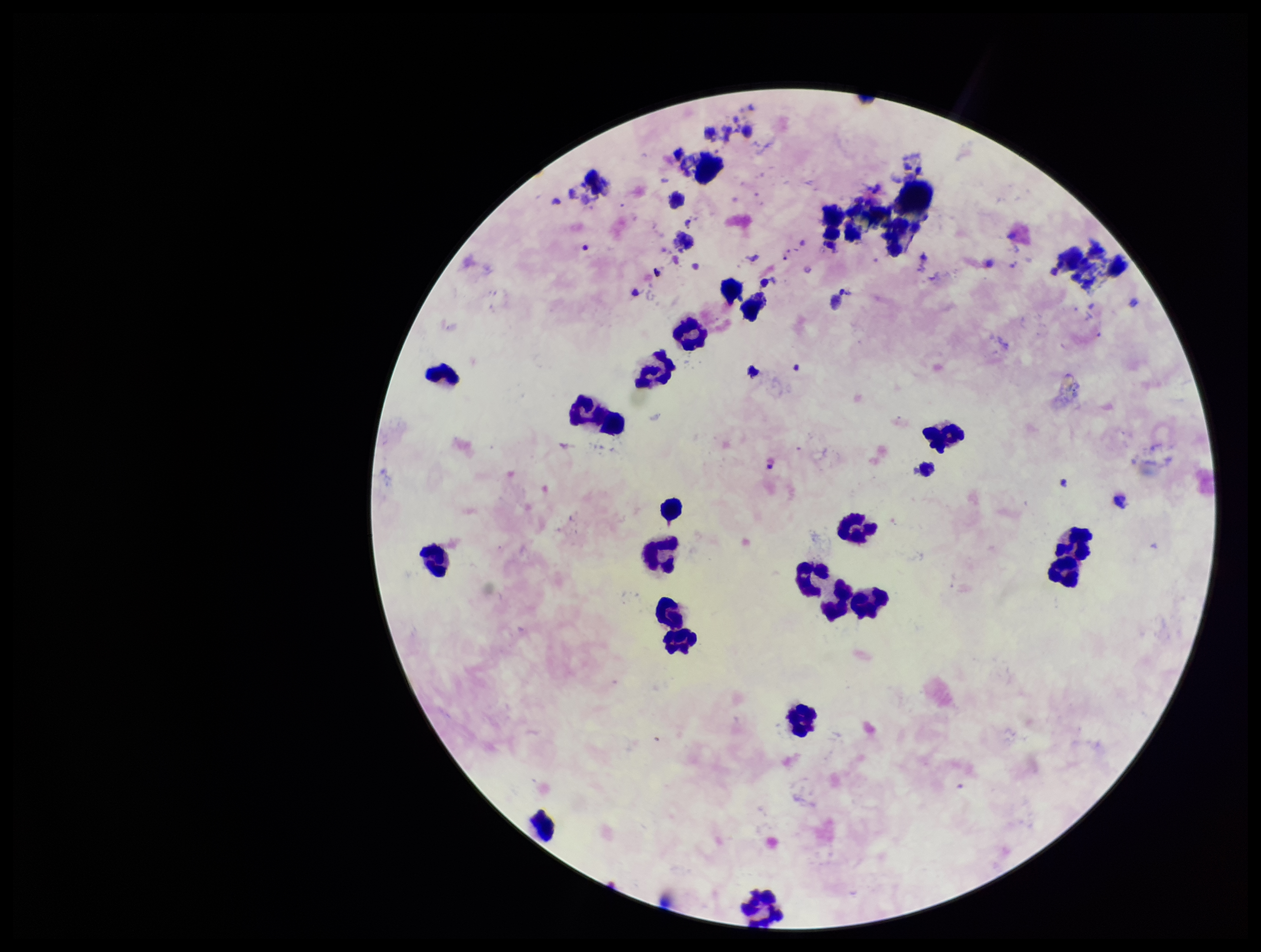

Summary:
  - Plasmodium parasites: none seen
  - Patient malaria status: negative
  - Image size: 1261×952 pixels
  - Preparation: thick
  - Leukocyte count: 20
  - Field of view: single
  - Parasite count: 0
  - Stain: Giemsa
  - Capture: smartphone photograph through the microscope eyepiece